Which red blood cells are P. falciparum-infected, and which are of indeterminate infection status?
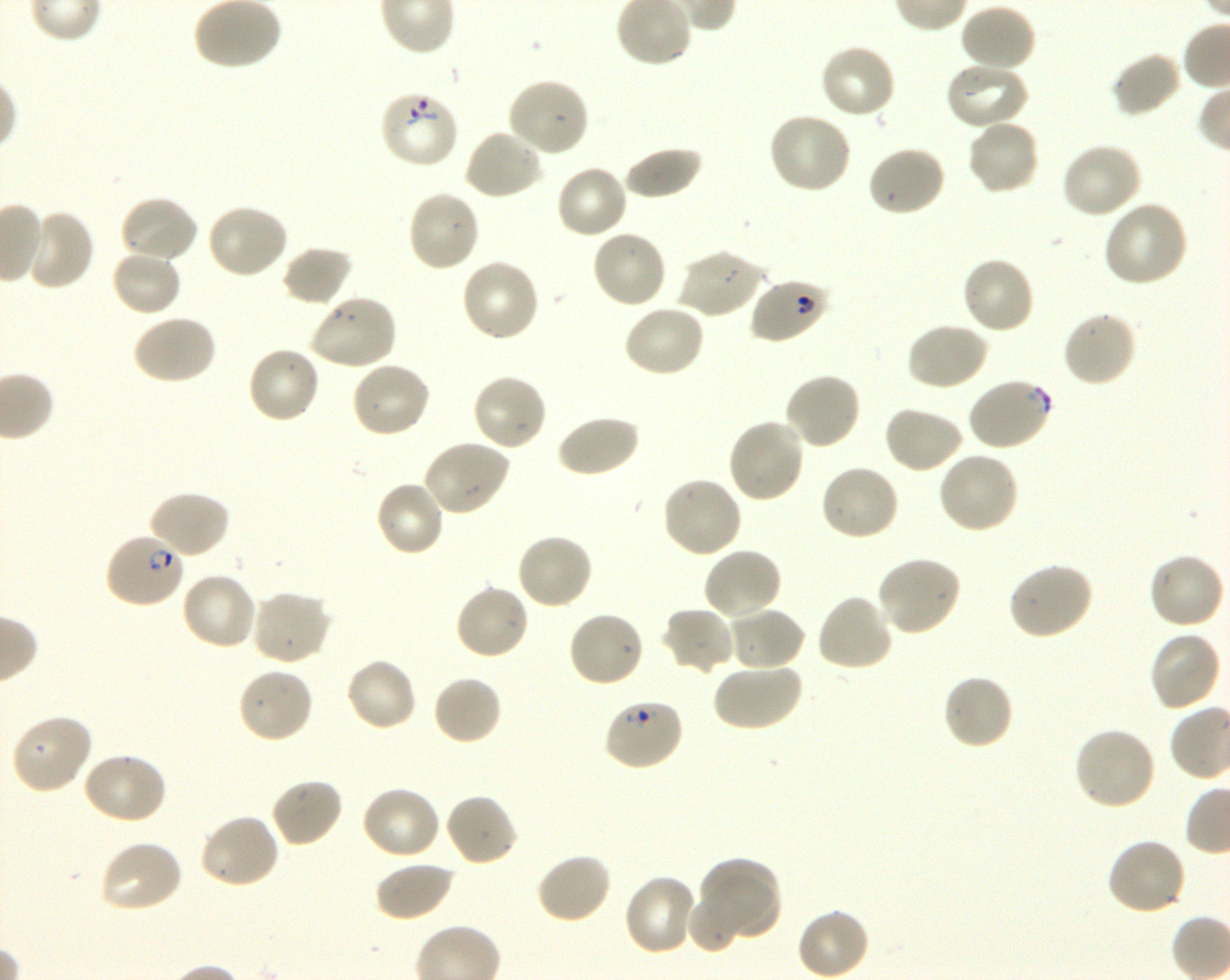
Approximate bounding boxes as (x1, y1, x2, y2) in pixels. Not every red blood cell is marked. A life-cycle stage — or a range of stages, where the recorded stages span more than one — follows each staged infected red blood cell.
Infected red blood cells: (104, 533, 186, 609) ring.
Red blood cells of indeterminate infection status: (378, 90, 459, 169), (750, 277, 829, 345), (967, 377, 1053, 452), (602, 697, 685, 772).

Locations of uninfected red blood cells: (959, 4, 1038, 74), (818, 43, 897, 121), (1111, 51, 1182, 118), (944, 62, 1030, 131), (506, 77, 590, 158), (767, 111, 852, 194), (965, 119, 1042, 196), (463, 128, 543, 200), (1060, 142, 1143, 220), (621, 144, 703, 201), (866, 145, 946, 217), (555, 163, 629, 239), (406, 189, 482, 273), (119, 194, 200, 265), (1103, 199, 1190, 287), (205, 203, 289, 279), (21, 207, 95, 292), (590, 229, 668, 309), (281, 245, 355, 306), (676, 248, 765, 319), (110, 250, 182, 317), (960, 256, 1036, 335), (461, 257, 541, 343), (307, 294, 398, 371), (622, 303, 706, 378), (1061, 309, 1139, 388), (131, 313, 218, 385), (905, 321, 988, 391), (246, 346, 321, 425), (350, 360, 432, 439), (783, 371, 862, 451), (471, 372, 548, 452), (883, 406, 965, 474), (555, 413, 640, 478), (726, 417, 806, 504), (422, 438, 511, 517), (936, 451, 1020, 535), (818, 464, 901, 543), (660, 475, 742, 559), (373, 479, 446, 558), (148, 489, 232, 560), (515, 532, 593, 611), (702, 546, 783, 621), (1148, 552, 1226, 631), (875, 555, 963, 636), (1007, 562, 1095, 640), (180, 571, 259, 651), (453, 583, 531, 661), (249, 589, 332, 667), (816, 592, 894, 672), (662, 606, 734, 675), (726, 606, 806, 672), (566, 610, 645, 689), (1148, 631, 1222, 712), (345, 657, 418, 732), (712, 661, 802, 732), (237, 666, 315, 745), (941, 672, 1015, 750), (432, 675, 503, 746), (10, 713, 94, 795), (1072, 726, 1157, 811), (80, 751, 168, 825), (270, 776, 344, 848), (361, 785, 442, 860), (444, 792, 519, 867), (199, 813, 281, 890), (1106, 837, 1187, 917), (98, 839, 183, 914), (534, 851, 612, 924), (697, 855, 783, 942), (374, 860, 455, 921), (623, 874, 700, 957), (686, 891, 746, 955), (796, 908, 870, 980). Blood group of the donor: O+. 100x oil-immersion objective, numerical aperture 1.30. Thin blood smear. Image is 1230×980 pixels. Giemsa-stained preparation. Shaking in-vitro culture of P. falciparum strain 3D7. Single field of view.